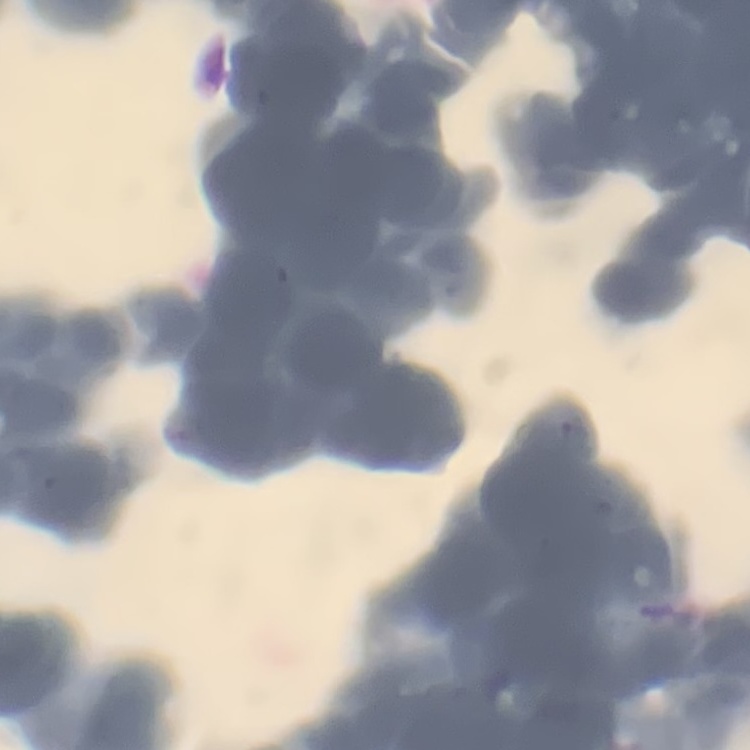
erythrocyte morphology = rouleaux formation
preparation = thin blood film
stain = Field's or Giemsa
image type = one tile cut from a larger photomicrograph